Locate and identify every blood parasite.
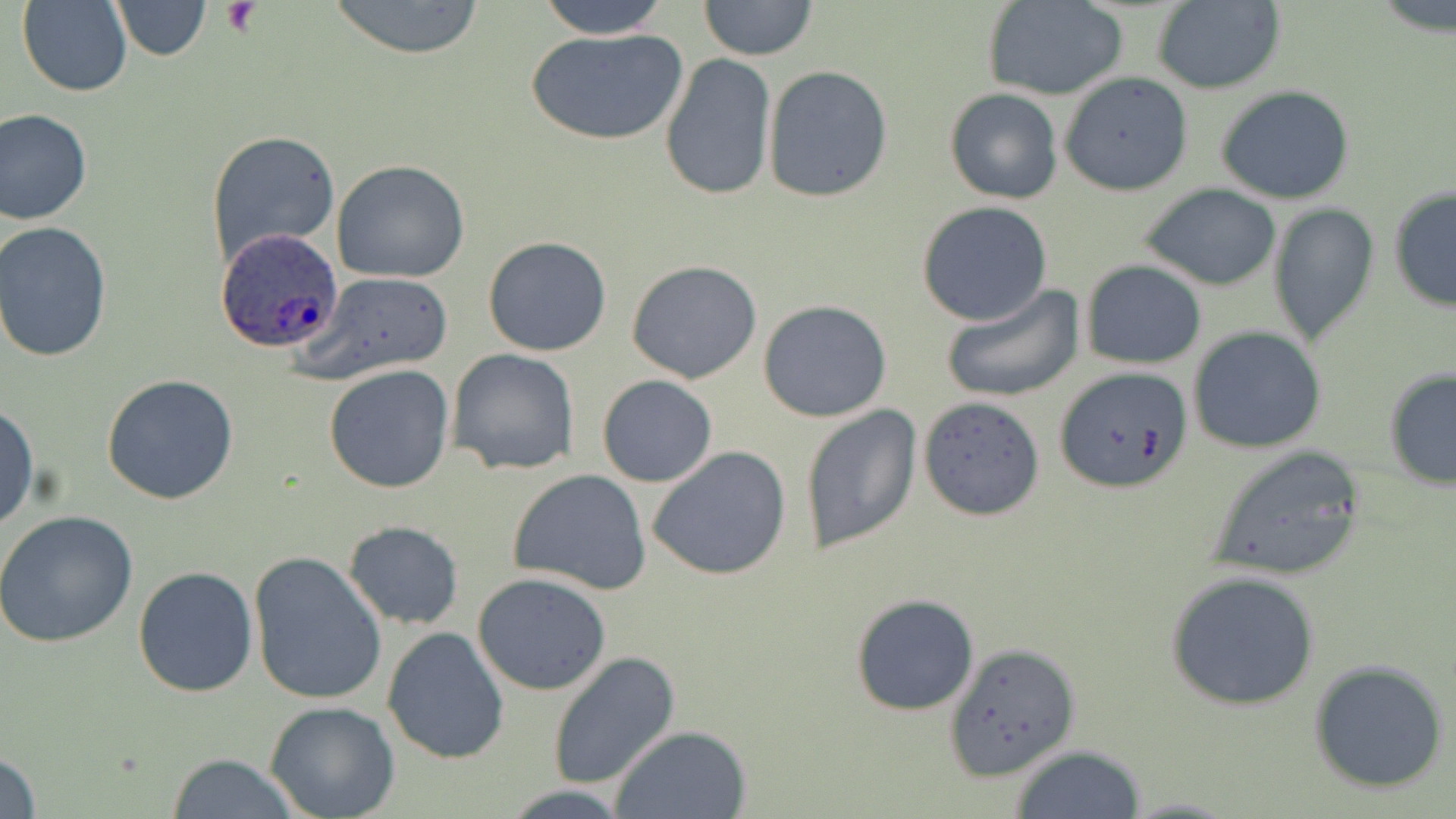

Approximate bounding boxes as named x1/y1/x2/y2 corners in pixels.
Plasmodium ovale-infected red blood cells: (x1=217, y1=229, x2=343, y2=355).
No Plasmodium falciparum, Plasmodium malariae, Plasmodium vivax, Babesia divergens, or Trypanosoma brucei observed.

slide_level_diagnosis: Plasmodium ovale
field_of_view: one of a larger specimen
image_size: 1456×819 pixels
stain: May-Grünwald-Giemsa
preparation: thin blood smear
platelet_locations: 'approximate bounding boxes as named x1/y1/x2/y2 corners in pixels: (x1=222, y1=2, x2=260, y2=37)'
uninfected_red_blood_cell_locations: 'approximate bounding boxes as named x1/y1/x2/y2 corners in pixels: (x1=327, y1=0, x2=489, y2=59), (x1=533, y1=0, x2=675, y2=40), (x1=698, y1=0, x2=818, y2=62), (x1=982, y1=0, x2=1131, y2=102), (x1=18, y1=1, x2=132, y2=97), (x1=110, y1=1, x2=212, y2=60), (x1=1150, y1=1, x2=1285, y2=94), (x1=526, y1=26, x2=689, y2=148), (x1=660, y1=54, x2=776, y2=201), (x1=763, y1=66, x2=894, y2=201), (x1=1058, y1=73, x2=1193, y2=196), (x1=943, y1=87, x2=1065, y2=204), (x1=1215, y1=87, x2=1355, y2=205), (x1=0, y1=108, x2=93, y2=226), (x1=205, y1=129, x2=342, y2=272), (x1=331, y1=160, x2=473, y2=283), (x1=1141, y1=185, x2=1282, y2=291), (x1=1387, y1=187, x2=1456, y2=313), (x1=915, y1=201, x2=1052, y2=325), (x1=1268, y1=201, x2=1380, y2=346), (x1=1, y1=222, x2=117, y2=363), (x1=483, y1=235, x2=612, y2=356), (x1=626, y1=259, x2=762, y2=384), (x1=1080, y1=260, x2=1207, y2=368), (x1=303, y1=272, x2=456, y2=386), (x1=937, y1=283, x2=1087, y2=405), (x1=758, y1=299, x2=892, y2=423), (x1=1188, y1=327, x2=1327, y2=454), (x1=446, y1=347, x2=581, y2=476), (x1=322, y1=364, x2=455, y2=495), (x1=1054, y1=366, x2=1192, y2=494), (x1=1383, y1=367, x2=1456, y2=490), (x1=101, y1=373, x2=240, y2=505), (x1=597, y1=374, x2=716, y2=487), (x1=919, y1=395, x2=1045, y2=520), (x1=0, y1=402, x2=39, y2=534), (x1=800, y1=403, x2=922, y2=556), (x1=646, y1=445, x2=792, y2=580), (x1=1206, y1=447, x2=1367, y2=580), (x1=507, y1=469, x2=653, y2=595), (x1=0, y1=512, x2=138, y2=649), (x1=342, y1=520, x2=464, y2=630), (x1=246, y1=552, x2=389, y2=706), (x1=132, y1=566, x2=259, y2=698), (x1=1164, y1=569, x2=1322, y2=711), (x1=473, y1=571, x2=613, y2=695), (x1=849, y1=593, x2=981, y2=717), (x1=381, y1=626, x2=510, y2=765), (x1=946, y1=644, x2=1079, y2=782), (x1=547, y1=652, x2=681, y2=791), (x1=1308, y1=660, x2=1450, y2=794), (x1=264, y1=701, x2=401, y2=819), (x1=609, y1=725, x2=752, y2=818), (x1=1007, y1=744, x2=1149, y2=819), (x1=1, y1=746, x2=43, y2=819), (x1=167, y1=752, x2=301, y2=819)'
magnification: 1000x
modality: optical microscopy